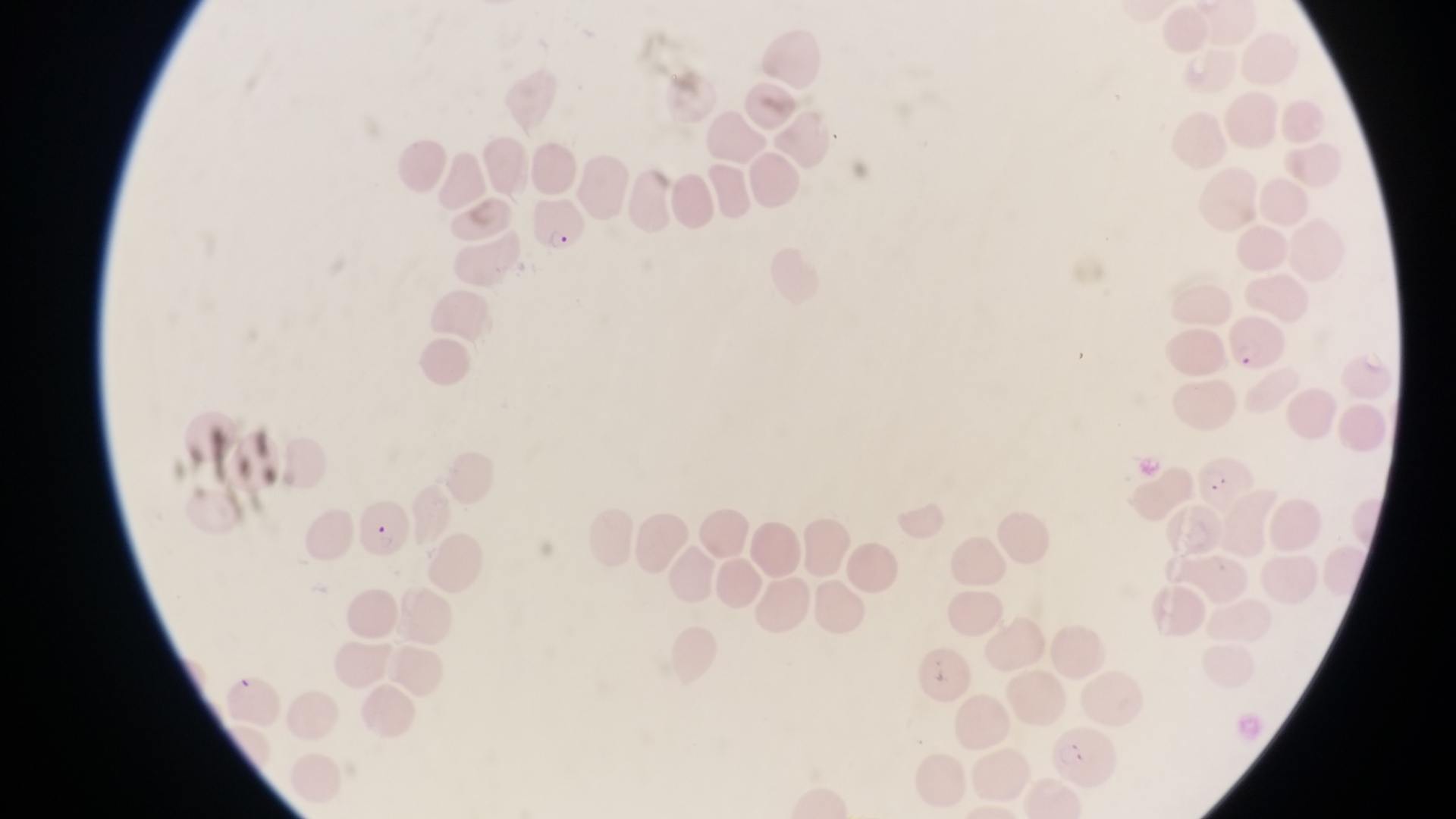

Approximate bounding boxes as {left, top, right, bottom} in pixels. Parasitised red blood cell locations: {535, 199, 588, 257}, {1222, 314, 1293, 374}, {1195, 449, 1253, 510}, {357, 502, 412, 563}. Collected in Uganda. Image is 1456×819 pixels. Magnification of 1000x. Thin blood film. Photographed through the eyepiece of an Olympus CX-23 microscope with a smartphone camera. Single field of view.